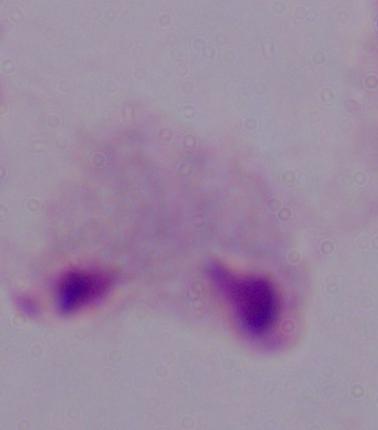 Captured at 1000x magnification. Micrograph. A trichomonad is shown.